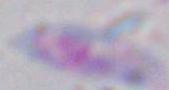

{
  "identification": "Toxoplasma gondii",
  "magnification": "1000x",
  "modality": "photomicrograph"
}